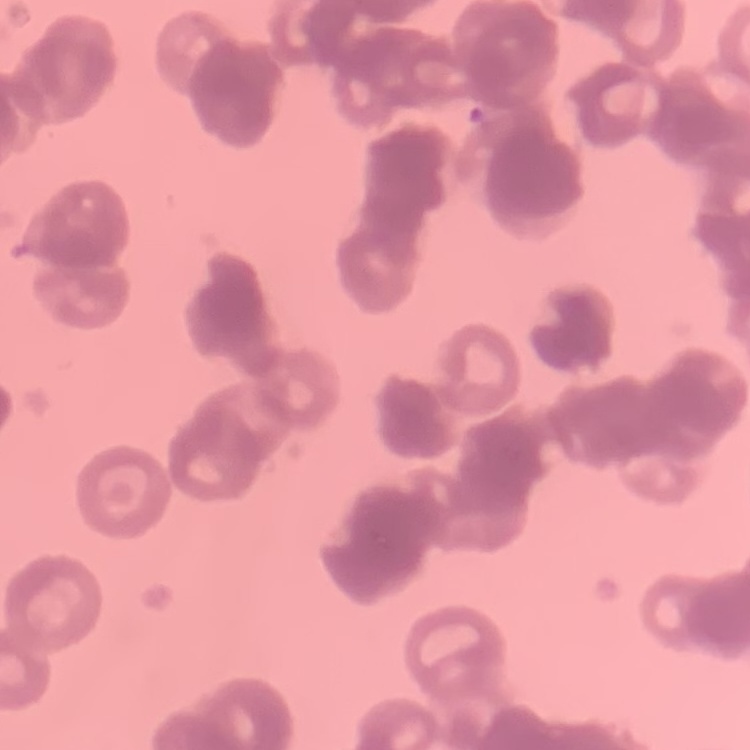 The red blood cells exhibit rouleaux formation. Thin peripheral smear. Square crop of a larger photomicrograph. Stained with either Field's or Giemsa.